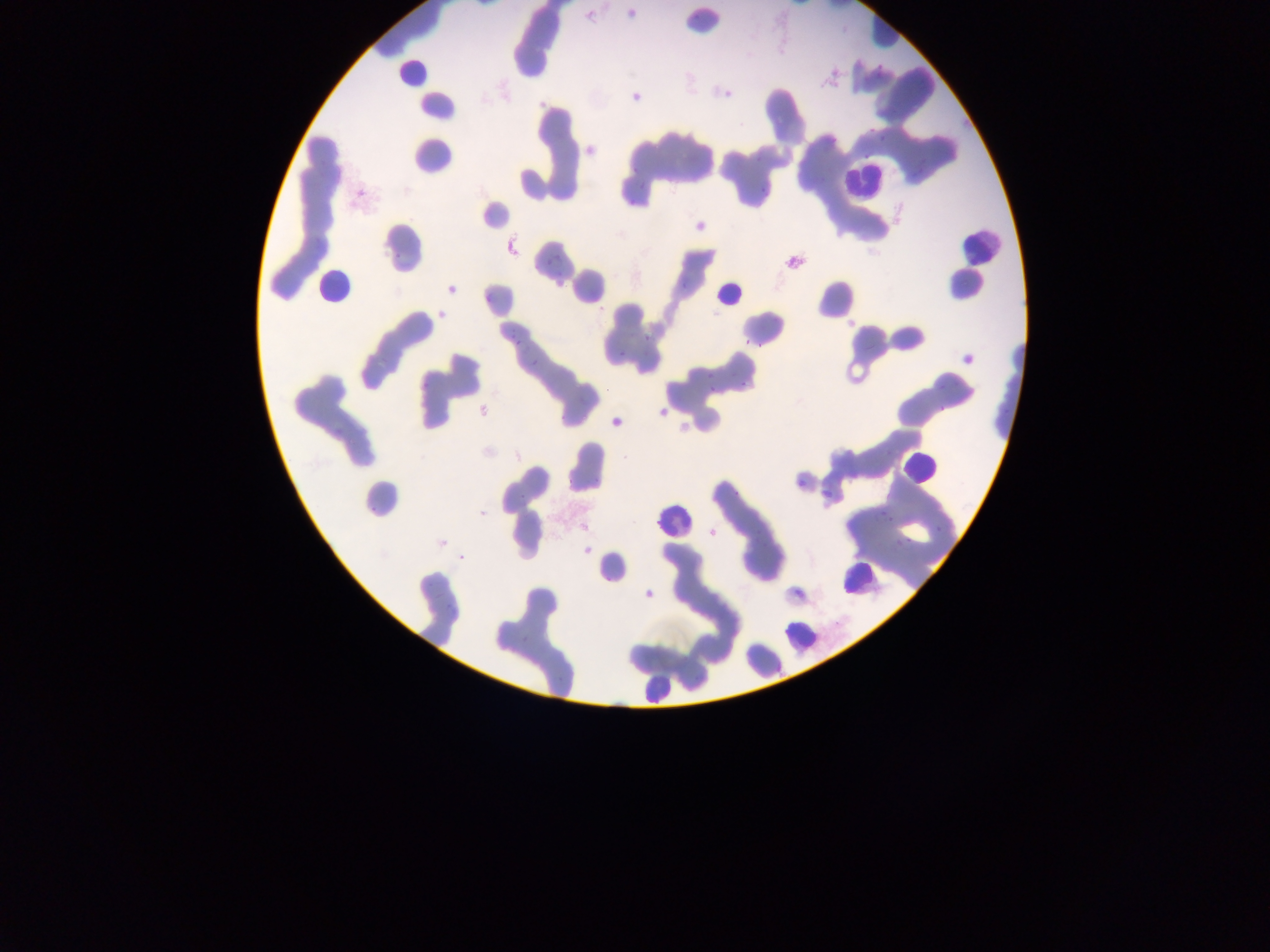

preparation = thin blood film
image size = 1270×952 pixels
country = Ghana
Plasmodium parasite locations = approximate bounding boxes as {left, top, right, bottom} in pixels: {623, 2, 644, 25}, {690, 11, 707, 19}, {878, 132, 889, 145}, {757, 189, 766, 194}, {543, 252, 558, 266}, {482, 292, 493, 301}, {503, 324, 517, 334}, {644, 334, 650, 343}, {743, 335, 756, 346}, {510, 340, 519, 350}, {618, 352, 628, 357}, {528, 358, 537, 366}, {738, 373, 749, 387}, {708, 385, 716, 393}, {934, 401, 950, 417}, {791, 470, 800, 491}, {819, 488, 836, 499}, {886, 516, 901, 523}, {935, 528, 943, 537}, {897, 537, 914, 549}, {433, 586, 447, 600}, {441, 602, 453, 614}, {515, 629, 534, 645} | approximate {x, y} pixel centers of objects too small to bound: {397, 255}, {882, 511}
field of view = single
capture = mobile-phone photograph through a microscope
leukocyte locations = approximate bounding boxes as {left, top, right, bottom} in pixels: {391, 58, 429, 91}, {845, 161, 881, 200}, {959, 232, 996, 265}, {316, 268, 352, 302}, {710, 277, 742, 317}, {901, 449, 933, 484}, {652, 502, 687, 538}, {836, 553, 874, 597}, {779, 618, 817, 650}, {641, 674, 667, 707}